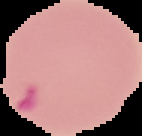
image size = 142×136 pixels
image type = segmented cell region on a black background
preparation = thin blood film
result = malaria parasites detected